Classify this cell by malaria status.
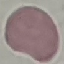
It is uninfected.

stain = Giemsa
image type = cell patch, automatically extracted from a larger field of view and resized to 64 × 64 pixels
preparation = thin smear
capture = smartphone camera at the microscope eyepiece